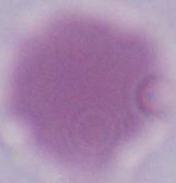
modality = micrograph
identification = erythrocyte
magnification = 1000x